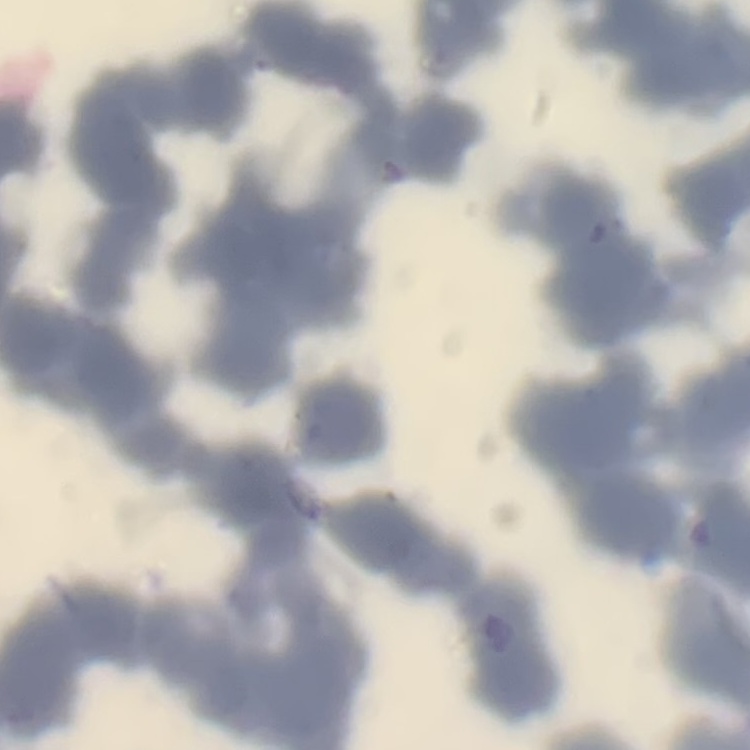
The red blood cells exhibit rouleaux formation. One tile cut from a larger photomicrograph. Thin blood smear. Stained with either Field's or Giemsa.